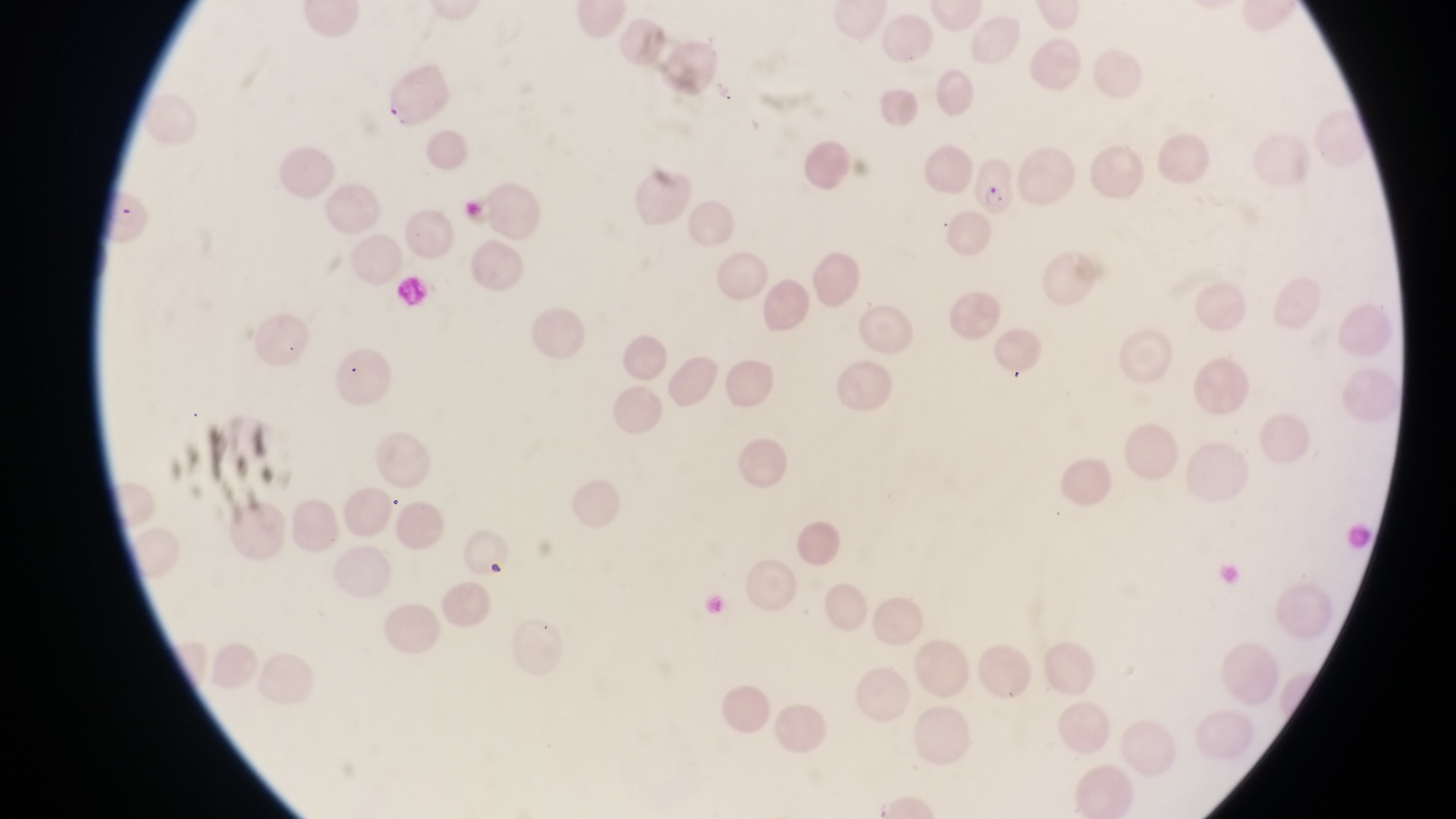

Approximate bounding boxes as [left, top, right, bottom] in pixels.
Summary:
  - Artifact (platelet-like body, stain precipitate, or debris) locations: [479, 555, 506, 576]
  - Parasitised red blood cell locations: [381, 77, 450, 129], [971, 155, 1018, 219]
  - Image size: 1456×819 pixels
  - Field of view: single
  - Capture: smartphone photograph through the eyepiece of an Olympus CX-23 microscope
  - Preparation: thin blood film
  - Magnification: 1000x
  - Country: Uganda